Assess this cell for malaria.
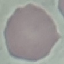

Uninfected.

{
  "stain": "Giemsa",
  "preparation": "thin blood smear",
  "image_type": "cell patch, automatically extracted from a larger field of view and resized to 64 × 64 pixels",
  "capture": "smartphone camera at the microscope eyepiece"
}